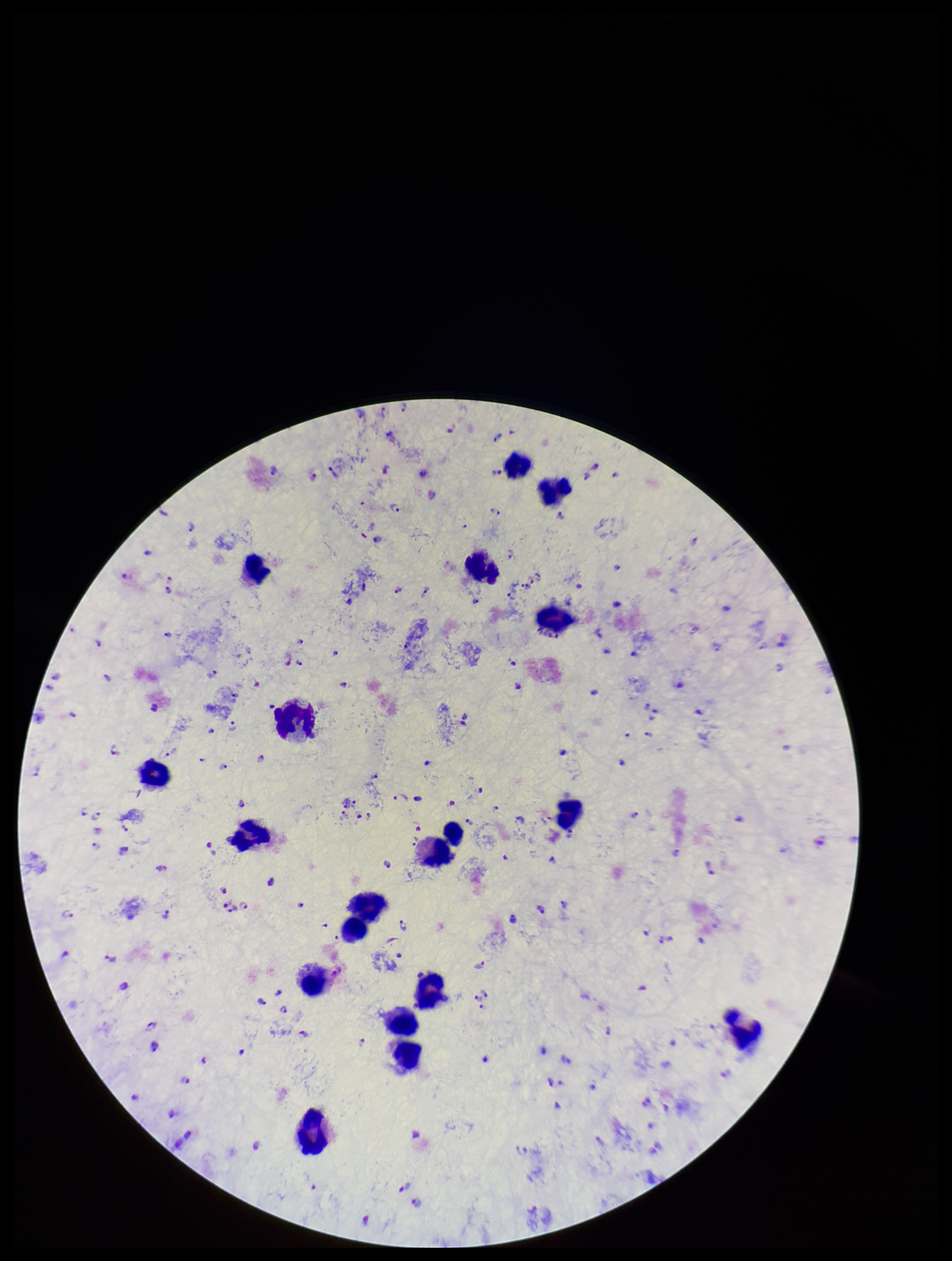
Leukocyte count: 18. One field from this slide. Parasite count: 172. Patient malaria status: positive. Preparation: thick. Plasmodium parasites: identified. Stained with Giemsa. Image is 952×1261 pixels. Smartphone photograph taken through the eyepiece of a microscope. Species reported for this patient: Plasmodium falciparum.